Name the cell type shown.
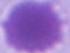

This is an erythrocyte.

magnification = 1000x
modality = micrograph